Outline each Plasmodium falciparum-infected red blood cell.
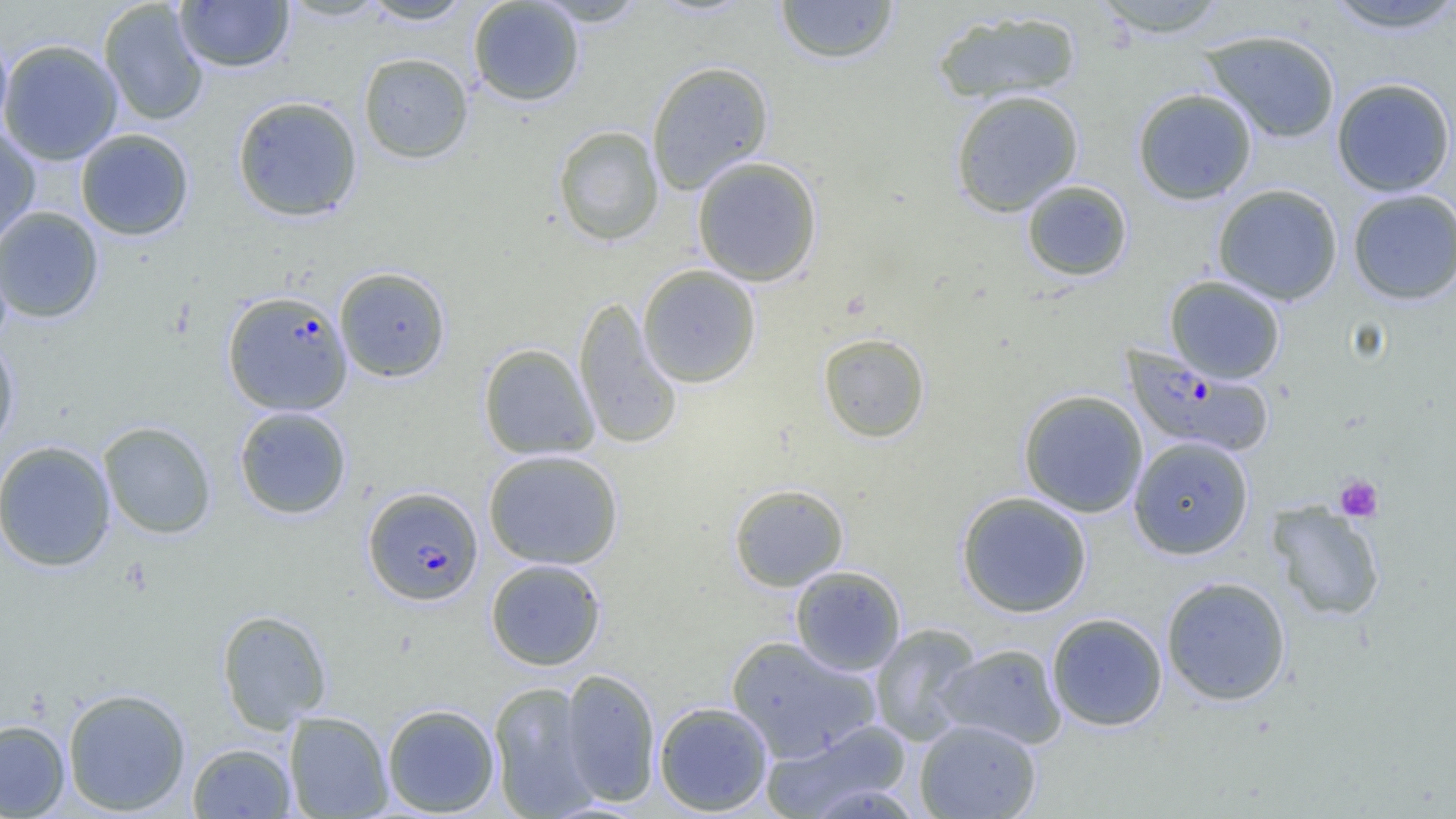

Approximate bounding boxes as named x1/y1/x2/y2 corners in pixels.
Plasmodium falciparum-infected red blood cells: (x1=222, y1=290, x2=352, y2=416), (x1=1122, y1=347, x2=1274, y2=459), (x1=363, y1=486, x2=483, y2=606).

Summary:
  - Uninfected red blood cell locations: (x1=280, y1=0, x2=390, y2=22), (x1=361, y1=0, x2=475, y2=25), (x1=468, y1=0, x2=585, y2=107), (x1=533, y1=0, x2=649, y2=27), (x1=775, y1=0, x2=899, y2=65), (x1=1090, y1=0, x2=1232, y2=38), (x1=99, y1=1, x2=209, y2=126), (x1=175, y1=1, x2=294, y2=72), (x1=1321, y1=1, x2=1456, y2=34), (x1=931, y1=8, x2=1083, y2=105), (x1=1200, y1=29, x2=1341, y2=144), (x1=0, y1=32, x2=13, y2=146), (x1=0, y1=39, x2=123, y2=165), (x1=358, y1=52, x2=473, y2=164), (x1=647, y1=60, x2=774, y2=194), (x1=1331, y1=77, x2=1455, y2=197), (x1=1132, y1=88, x2=1258, y2=205), (x1=950, y1=89, x2=1084, y2=217), (x1=232, y1=95, x2=363, y2=222), (x1=553, y1=125, x2=664, y2=246), (x1=0, y1=127, x2=40, y2=247), (x1=76, y1=128, x2=194, y2=241), (x1=692, y1=156, x2=823, y2=287), (x1=1021, y1=180, x2=1133, y2=281), (x1=1212, y1=184, x2=1343, y2=305), (x1=1347, y1=189, x2=1456, y2=305), (x1=0, y1=206, x2=104, y2=323), (x1=637, y1=265, x2=761, y2=388), (x1=334, y1=266, x2=451, y2=382), (x1=1164, y1=275, x2=1286, y2=383), (x1=573, y1=296, x2=683, y2=450), (x1=817, y1=332, x2=931, y2=443), (x1=0, y1=335, x2=20, y2=453), (x1=478, y1=343, x2=599, y2=461), (x1=1018, y1=389, x2=1149, y2=517), (x1=234, y1=406, x2=351, y2=519), (x1=98, y1=421, x2=216, y2=539), (x1=1128, y1=436, x2=1254, y2=559), (x1=0, y1=440, x2=116, y2=572), (x1=483, y1=449, x2=623, y2=569), (x1=728, y1=483, x2=849, y2=591), (x1=956, y1=491, x2=1092, y2=618), (x1=1267, y1=502, x2=1385, y2=621), (x1=485, y1=559, x2=606, y2=671), (x1=790, y1=565, x2=906, y2=676), (x1=1160, y1=576, x2=1292, y2=706), (x1=216, y1=609, x2=332, y2=732), (x1=1046, y1=612, x2=1168, y2=732), (x1=869, y1=623, x2=983, y2=746), (x1=725, y1=635, x2=881, y2=762), (x1=937, y1=643, x2=1066, y2=749), (x1=560, y1=668, x2=660, y2=806), (x1=488, y1=681, x2=600, y2=818), (x1=62, y1=687, x2=192, y2=816), (x1=653, y1=701, x2=773, y2=816), (x1=382, y1=703, x2=500, y2=816), (x1=284, y1=711, x2=393, y2=818), (x1=760, y1=718, x2=913, y2=819), (x1=0, y1=719, x2=70, y2=818), (x1=915, y1=719, x2=1041, y2=819), (x1=187, y1=742, x2=296, y2=818)
  - Platelet locations: (x1=1334, y1=474, x2=1384, y2=523)
  - Slide-level diagnosis: Plasmodium falciparum
  - Modality: optical microscopy
  - Image size: 1456×819 pixels
  - Magnification: 1000x
  - Preparation: thin blood smear
  - Field of view: single